State which cell type is depicted.
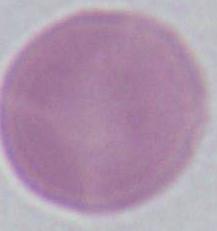

This is an erythrocyte.

Summary:
  - Modality: photomicrograph
  - Magnification: 1000x